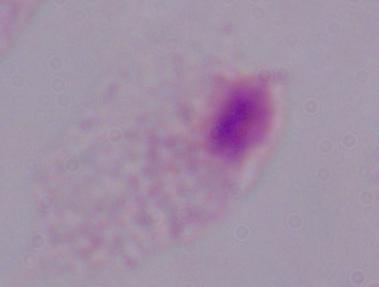
Captured at 1000x magnification. A trichomonad is shown. Photomicrograph.